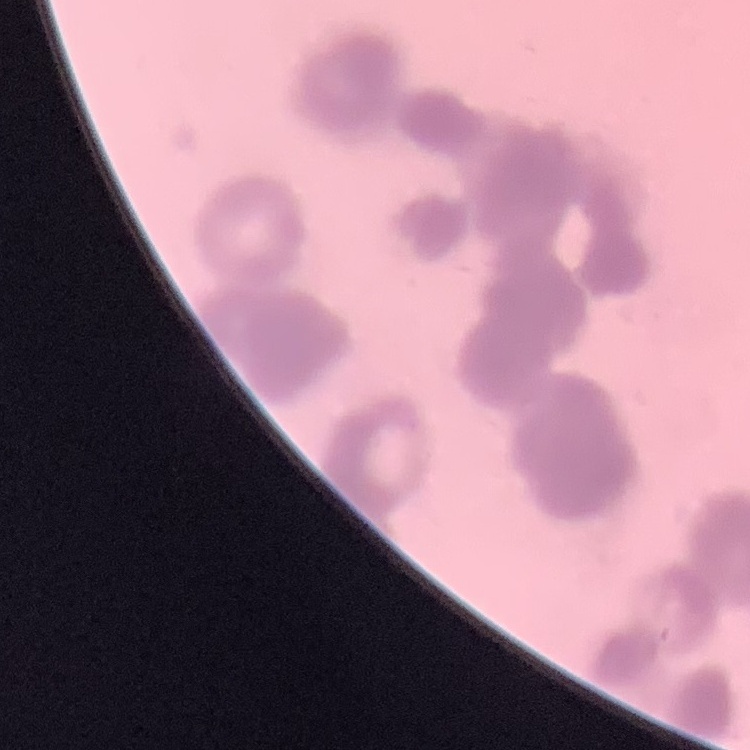 The red blood cells exhibit rouleaux formation. Square crop of a larger photomicrograph. Thin peripheral smear. Stained with either Field's or Giemsa.